Locate every Plasmodium parasite.
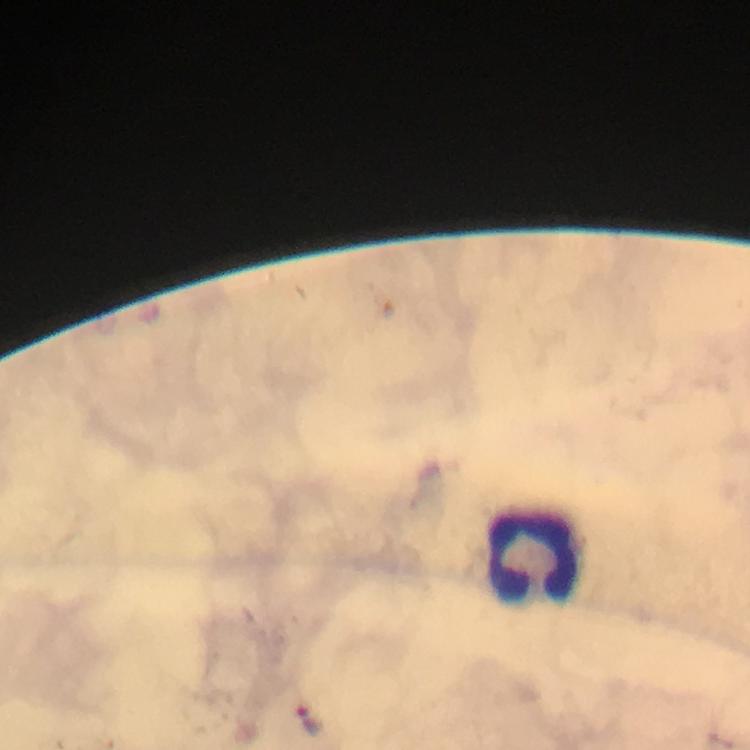
Approximate centers as (x, y) in pixels.
Plasmodium parasites: (310, 721).

Leukocyte locations: (534, 554). Photographed through the microscope with a smartphone camera. From a diagnostic examination for malaria. Giemsa stain. 100x magnification. Image is 750×750 pixels. A crop from one field of view. Immersion oil applied. Thick blood smear.